Identify the parasite.
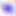

Toxoplasma gondii.

magnification = 400x
modality = photomicrograph